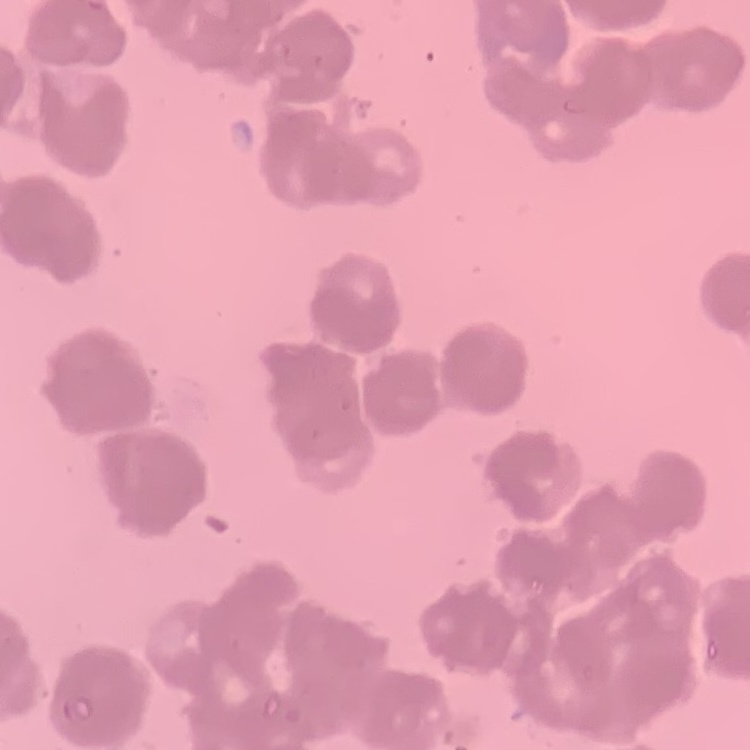
Summary:
  - Red blood cell morphology: rouleaux formation
  - Image type: one tile cut from a larger photomicrograph
  - Stain: Field's or Giemsa
  - Preparation: thin peripheral smear